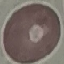
Summary:
  - Result: negative for malaria parasites
  - Stain: Giemsa
  - Capture: smartphone through the microscope eyepiece
  - Image type: automatically extracted cell patch, resized to 64 × 64 pixels
  - Preparation: thin blood smear